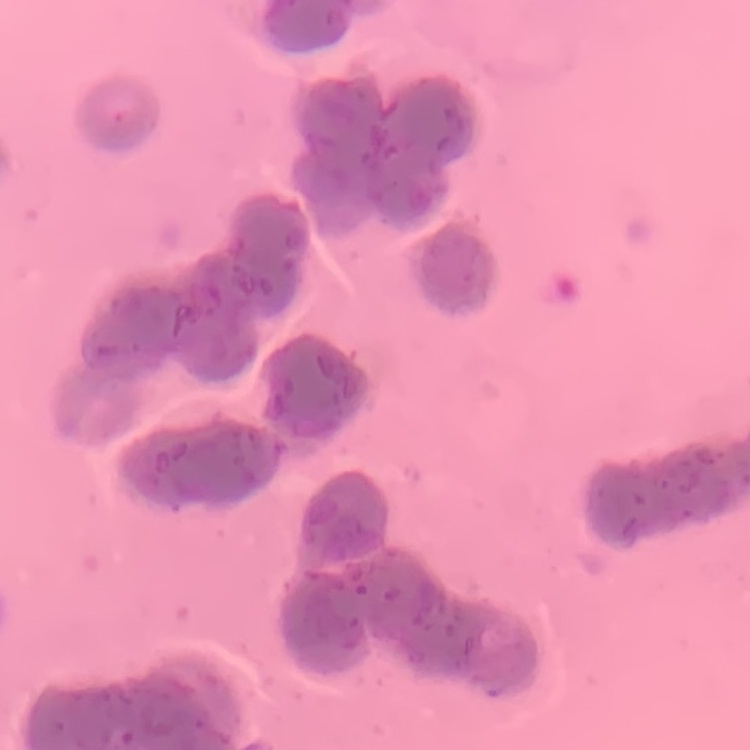

Summary:
  - Erythrocyte morphology: rouleaux formation
  - Preparation: thin blood smear
  - Image type: one tile cut from a larger photomicrograph
  - Stain: Field's or Giemsa